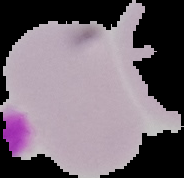
Summary:
  - Preparation: thin blood smear
  - Image type: segmented cell region with the area outside set to black
  - Result: no malaria parasites detected
  - Image size: 184×178 pixels